Identify the cell.
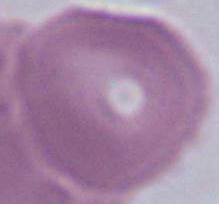
This is an erythrocyte.

Captured at 1000x magnification. Micrograph.